Locate every malaria parasite.
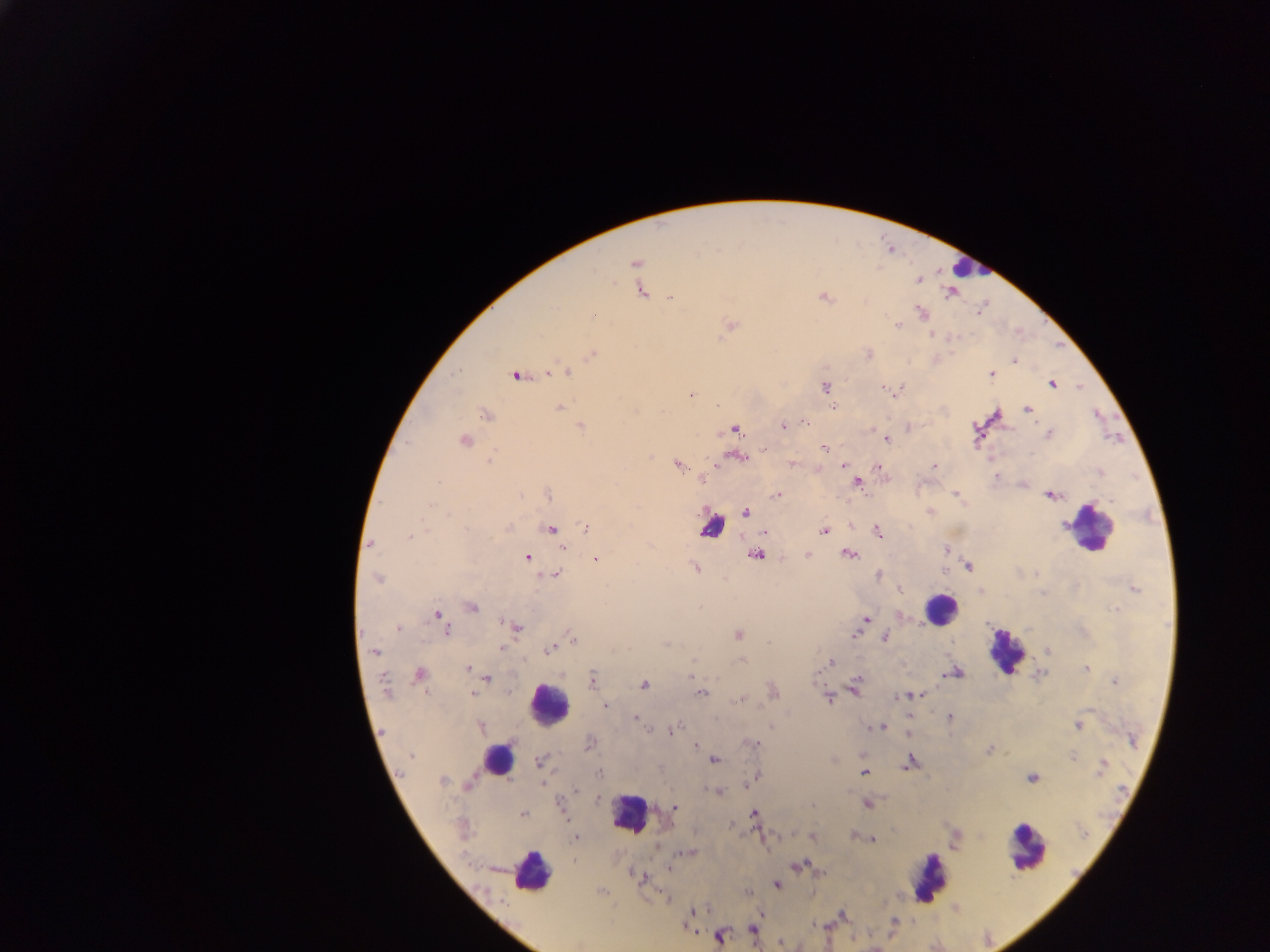

Approximate centers as x y in pixels.
Malaria parasites: 718 250; 634 263; 613 281; 639 289; 949 294; 823 297; 669 298; 922 312; 898 326; 730 327; 932 334; 592 355; 1014 361; 567 373; 992 374; 515 375; 548 375; 1052 385; 824 388; 885 388; 691 393; 558 408; 835 408; 1026 408; 483 414; 994 416; 805 423; 580 425; 782 425; 736 429; 1049 433; 465 439; 886 439; 823 448; 738 456; 488 459; 728 459; 792 463; 679 465; 845 465; 877 465; 933 465; 1099 473; 997 476; 702 477; 439 481; 859 481; 547 495; 778 495; 956 495; 1050 496; 1110 499; 431 504; 747 512; 930 512; 507 526; 585 528; 552 530; 878 530; 763 532; 825 532; 407 535; 369 545; 563 548; 946 551; 755 554; 807 554; 848 554; 597 558; 528 559; 968 566; 697 567; 1037 573; 557 574; 877 575; 378 580; 899 587; 1136 589; 980 590; 474 607; 1114 609; 437 614; 866 620; 499 622; 503 623; 519 629; 400 630; 448 630; 737 634; 853 636; 884 638; 573 640; 665 644; 502 647; 548 650; 375 652; 1050 653; 694 659; 741 660; 831 661; 1085 668; 467 669; 814 674; 418 676; 690 676; 487 679; 592 679; 1115 681; 384 683; 855 683; 644 684; 774 692; 472 693; 702 694; 854 694; 925 694; 904 696; 912 696; 898 697; 739 699; 828 700; 605 706; 636 716; 949 717; 481 726; 1076 726; 866 727; 883 727; 670 732; 905 737; 695 744; 987 751; 411 755; 1072 757; 714 759; 909 760; 539 761; 1103 763; 906 766; 1100 770; 400 772; 864 773; 1033 779; 441 781; 543 781; 468 785; 465 788; 576 788; 719 791; 867 804; 812 805; 674 807; 754 813; 521 814; 813 836; 854 837; 575 838; 874 839; 685 853; 795 866; 667 869; 640 876; 776 885; 666 898; 692 908; 843 915; 899 920; 754 929; 719 937.

image size = 1270×952 pixels
country = Ghana
preparation = thick blood smear
field of view = single
capture = mobile-phone photograph through a microscope